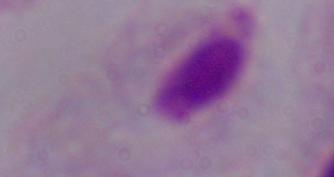

modality = photomicrograph
identification = trichomonad
magnification = 1000x